Assess the morphology of the red blood cells.
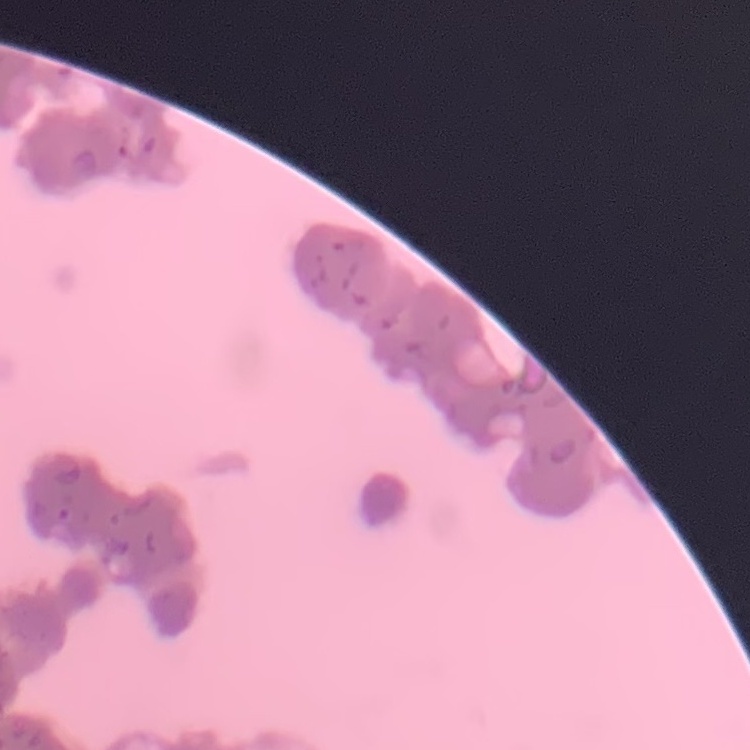

Rouleaux formation.

One tile cut from a larger photomicrograph. Thin blood smear. Stained with either Field's or Giemsa.